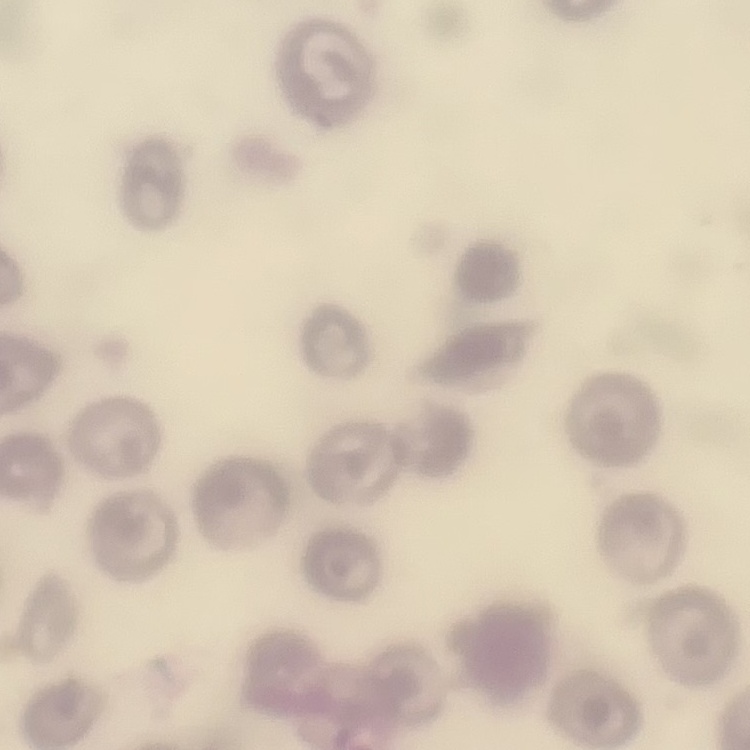

{
  "red_blood_cell_morphology": "no rouleaux formation",
  "stain": "Field's or Giemsa",
  "preparation": "thin blood smear",
  "image_type": "square crop of a larger photomicrograph"
}